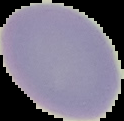

Summary:
  - Image type: cell region segmented out of the field of view; surrounding area masked to black
  - Image size: 124×121 pixels
  - Preparation: thin blood smear
  - Malaria status: uninfected